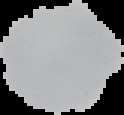

Summary:
  - Image size: 124×115 pixels
  - Image type: segmented cell region on a black background
  - Preparation: thin blood film
  - Result: negative for malaria parasites